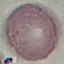
Malaria status: uninfected. Photographed with a smartphone camera at the microscope eyepiece. Thin blood film. Giemsa stain. Automatically extracted cell patch, resized to 64 × 64 pixels.